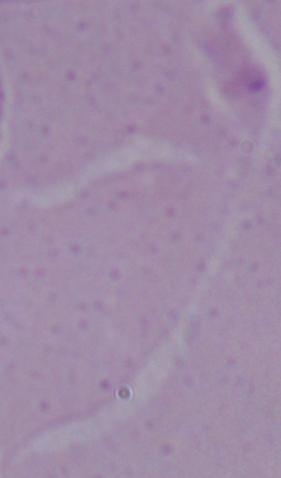

Summary:
  - Magnification: 1000x
  - Identification: Leishmania
  - Modality: photomicrograph